Comment on the morphology of the erythrocytes.
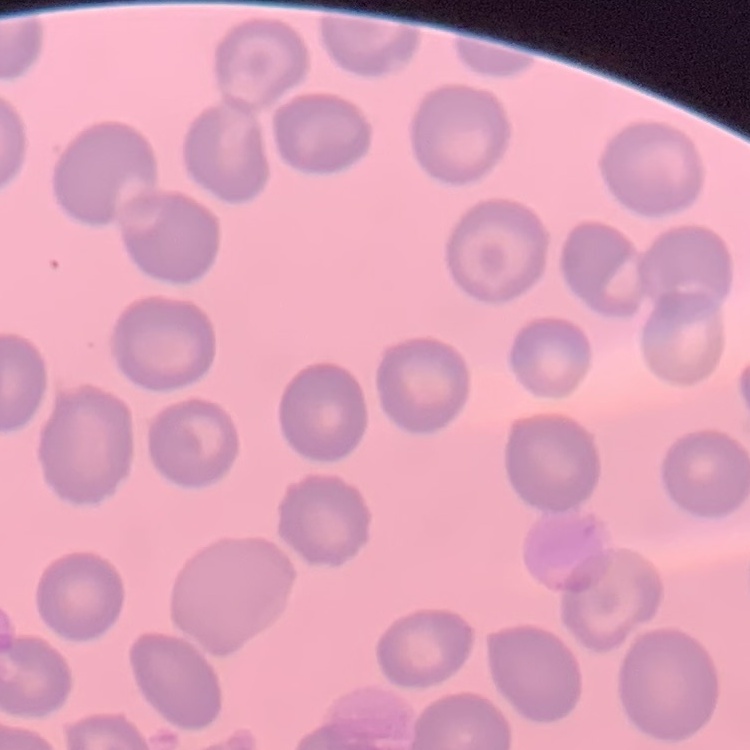

No rouleaux formation.

image_type: square crop of a larger photomicrograph
preparation: thin peripheral smear
stain: Field's or Giemsa